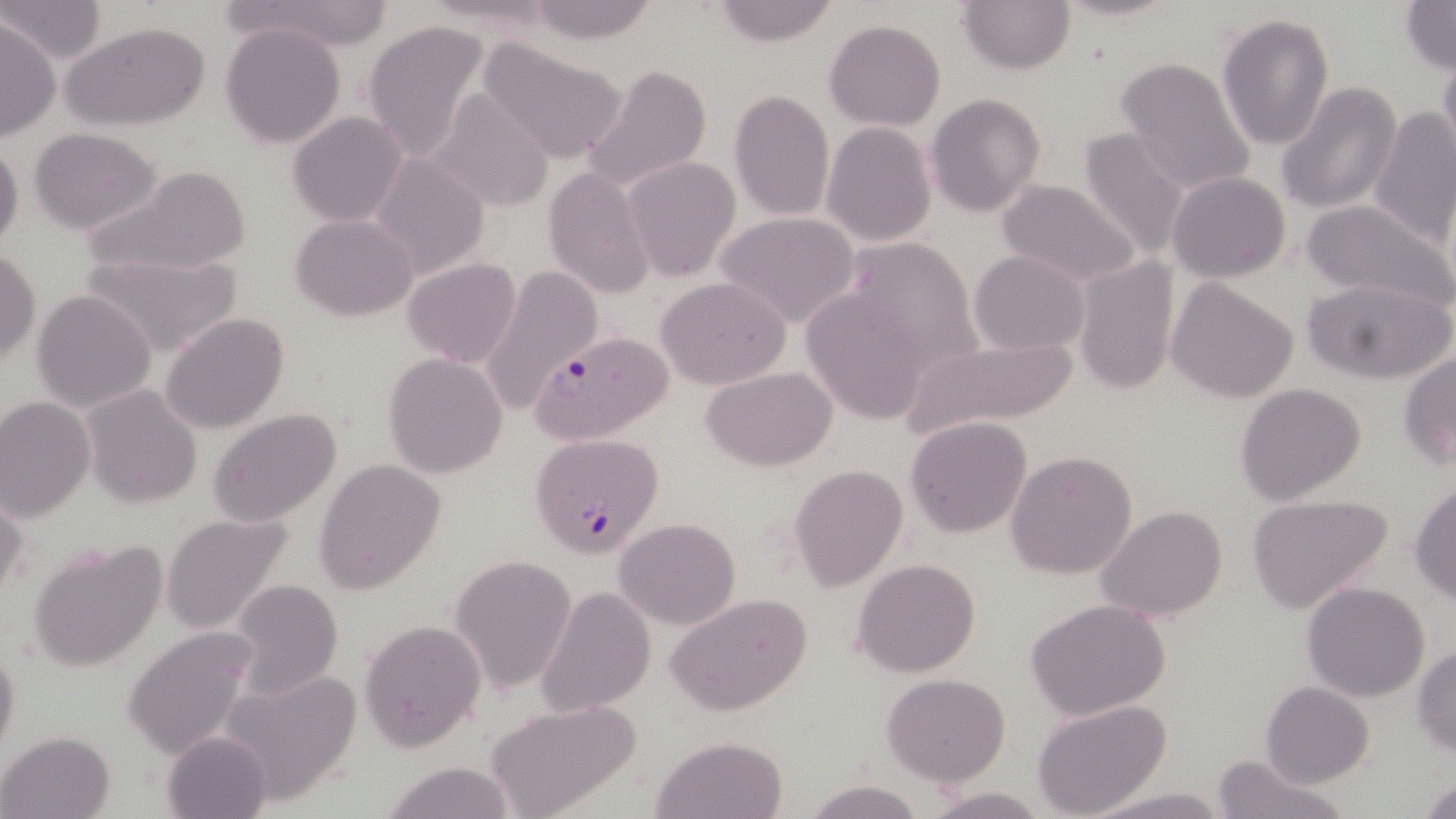

slide_level_diagnosis: Plasmodium falciparum
preparation: thin blood film
magnification: 1000x
image_size: 1456×819 pixels
modality: optical microscopy
plasmodium_falciparum_infected_red_blood_cell_locations: 'approximate bounding boxes as (x1, y1, x2, y2) in pixels: (529, 332, 676, 446), (530, 433, 664, 557)'
field_of_view: single
stain: May-Grünwald-Giemsa
uninfected_red_blood_cell_locations: 'approximate bounding boxes as (x1, y1, x2, y2) in pixels: (0, 0, 104, 62), (956, 0, 1075, 74), (1053, 0, 1182, 23), (257, 1, 394, 50), (705, 1, 844, 47), (1400, 1, 1455, 74), (520, 2, 665, 44), (1216, 11, 1334, 151), (0, 17, 58, 140), (825, 18, 945, 130), (360, 19, 492, 164), (220, 21, 347, 149), (62, 22, 211, 131), (475, 38, 629, 163), (1438, 45, 1456, 167), (1114, 55, 1258, 196), (579, 62, 714, 192), (1276, 83, 1403, 213), (426, 87, 558, 212), (728, 90, 835, 221), (926, 93, 1046, 217), (1368, 108, 1456, 246), (287, 111, 409, 228), (821, 123, 937, 246), (1075, 126, 1195, 266), (29, 128, 162, 233), (0, 138, 24, 257), (370, 154, 491, 280), (622, 157, 741, 280), (86, 164, 252, 277), (541, 166, 654, 301), (1168, 172, 1291, 282), (994, 180, 1142, 289), (1301, 199, 1453, 311), (714, 212, 861, 328), (292, 214, 418, 321), (839, 239, 983, 372), (1, 250, 40, 364), (967, 250, 1092, 356), (84, 251, 242, 356), (1071, 255, 1181, 399), (401, 259, 523, 367), (478, 266, 600, 414), (655, 276, 791, 389), (1301, 276, 1453, 386), (1165, 277, 1300, 404), (800, 286, 937, 424), (30, 289, 158, 414), (160, 312, 291, 435), (896, 334, 1086, 444), (1398, 351, 1456, 471), (381, 353, 508, 478), (700, 365, 840, 472), (1234, 381, 1367, 505), (80, 384, 203, 509), (0, 397, 95, 519), (209, 409, 342, 526), (905, 417, 1033, 537), (1005, 449, 1138, 578), (315, 457, 445, 594), (789, 464, 908, 589), (1408, 481, 1456, 603), (0, 487, 26, 607), (1245, 492, 1395, 614), (1096, 505, 1229, 625), (159, 512, 298, 637), (612, 516, 741, 630), (27, 537, 167, 672), (448, 554, 578, 693), (852, 558, 981, 677), (226, 580, 344, 700), (1301, 581, 1431, 702), (535, 585, 655, 719), (667, 594, 812, 718), (1026, 599, 1171, 721), (360, 619, 486, 751), (121, 625, 259, 759), (0, 644, 21, 764), (1411, 645, 1456, 757), (217, 668, 364, 805), (881, 675, 1010, 786), (1260, 682, 1376, 788), (1031, 699, 1174, 819), (486, 700, 643, 817), (2, 730, 114, 817), (162, 732, 272, 818), (649, 735, 789, 818), (1212, 751, 1347, 819), (379, 760, 520, 819), (1419, 777, 1456, 818), (801, 778, 926, 819), (921, 786, 1048, 818), (1092, 788, 1229, 819)'